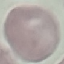

Summary:
  - Malaria status: uninfected
  - Image type: cell patch, automatically extracted from a larger field of view and resized to 64 × 64 pixels
  - Preparation: thin blood smear
  - Stain: Giemsa
  - Capture: smartphone through the microscope eyepiece